Assess this cell for malaria.
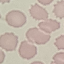

Uninfected.

Summary:
  - Image type: cell patch, automatically extracted from a larger field of view and resized to 64 × 64 pixels
  - Preparation: thin blood smear
  - Capture: smartphone through the microscope eyepiece
  - Stain: Giemsa